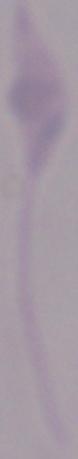
magnification: 1000x
identification: Leishmania
modality: micrograph